Locate every Plasmodium parasite.
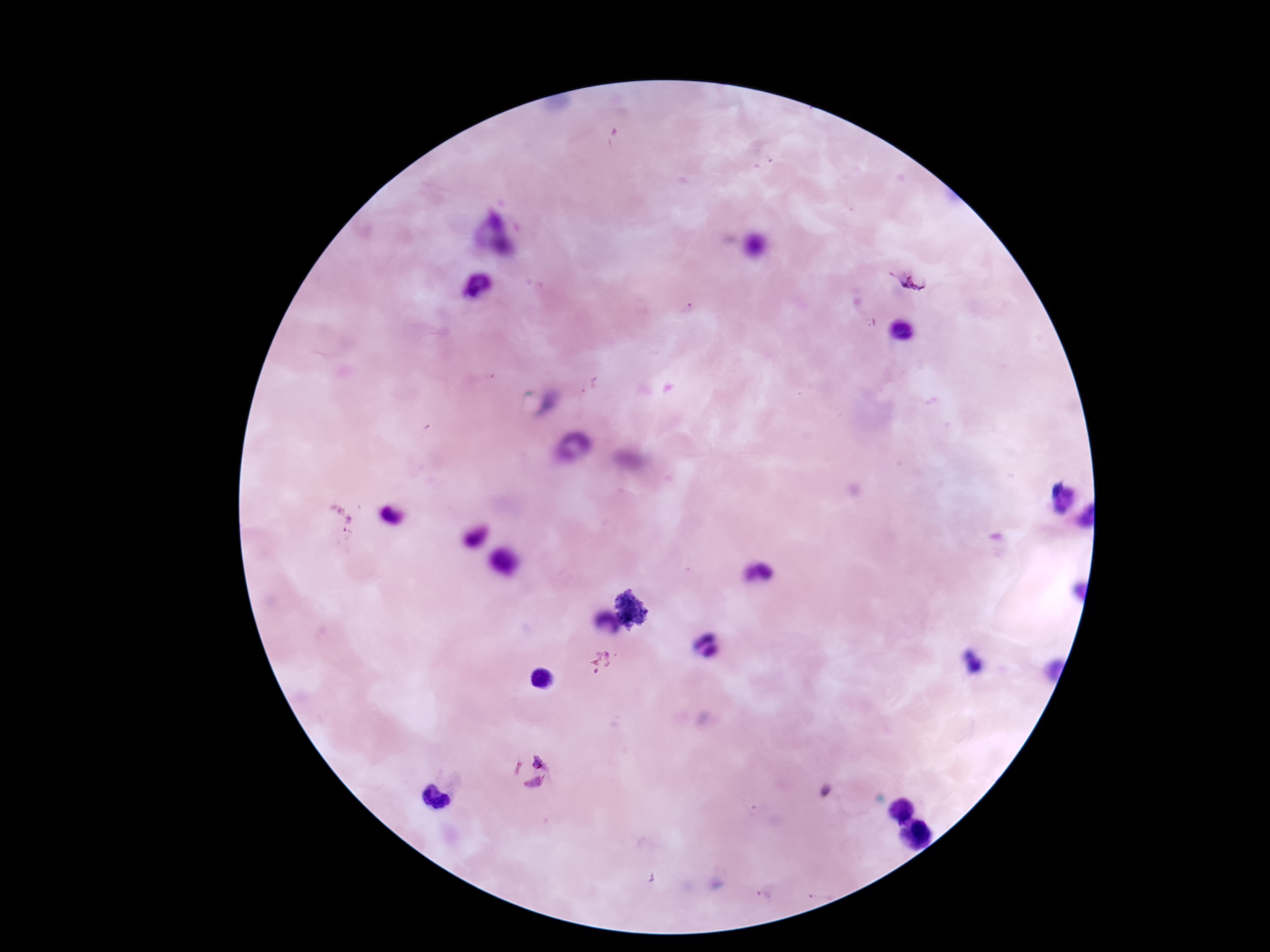

Approximate centers as {x, y} in pixels.
Plasmodium parasites: {913, 282}, {688, 309}, {590, 386}, {603, 664}, {531, 776}.

Summary:
  - Patient malaria status: infected
  - Stain: Giemsa
  - Capture: smartphone camera through the microscope eyepiece
  - Magnification: 100x
  - Preparation: thick blood film
  - Field of view: single
  - Image size: 1270×952 pixels